Comment on the morphology of the erythrocytes.
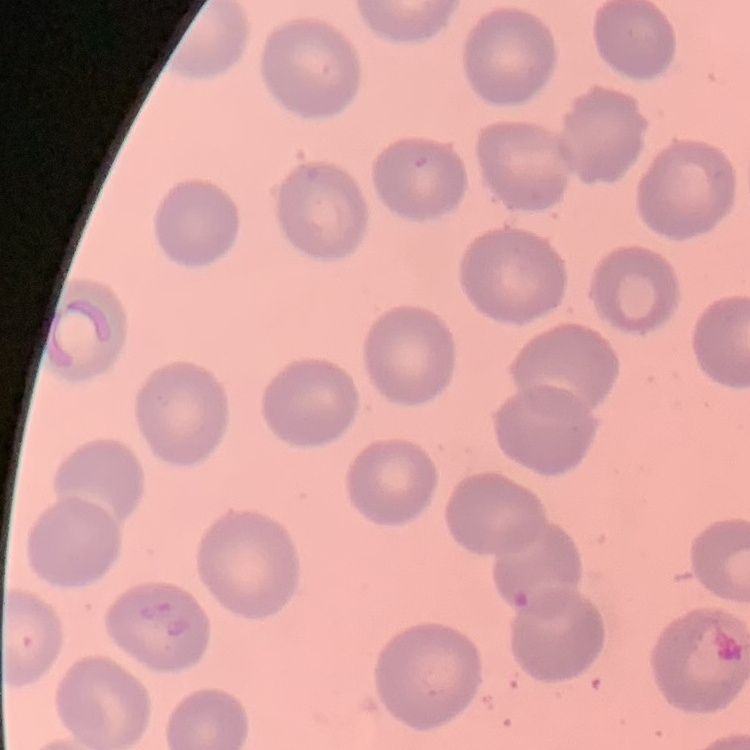
They show no rouleaux formation.

stain: Field's or Giemsa
image_type: square crop of a larger photomicrograph
preparation: thin peripheral smear